Report the malaria status of this cell.
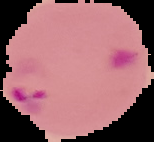

Parasitized.

Summary:
  - Image type: segmented cell region with the area outside set to black
  - Image size: 154×142 pixels
  - Preparation: thin blood film